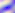
identification = Toxoplasma gondii
modality = micrograph
magnification = 400x